Comment on the morphology of the erythrocytes.
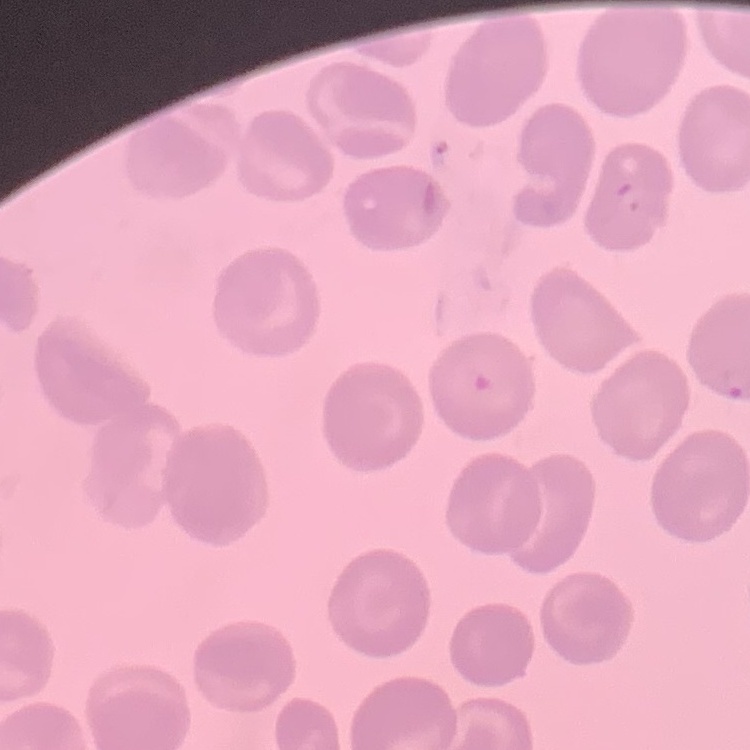

They show no rouleaux formation.

{
  "stain": "Field's or Giemsa",
  "preparation": "thin blood smear",
  "image_type": "square crop of a larger photomicrograph"
}